Identify the blood parasite species.
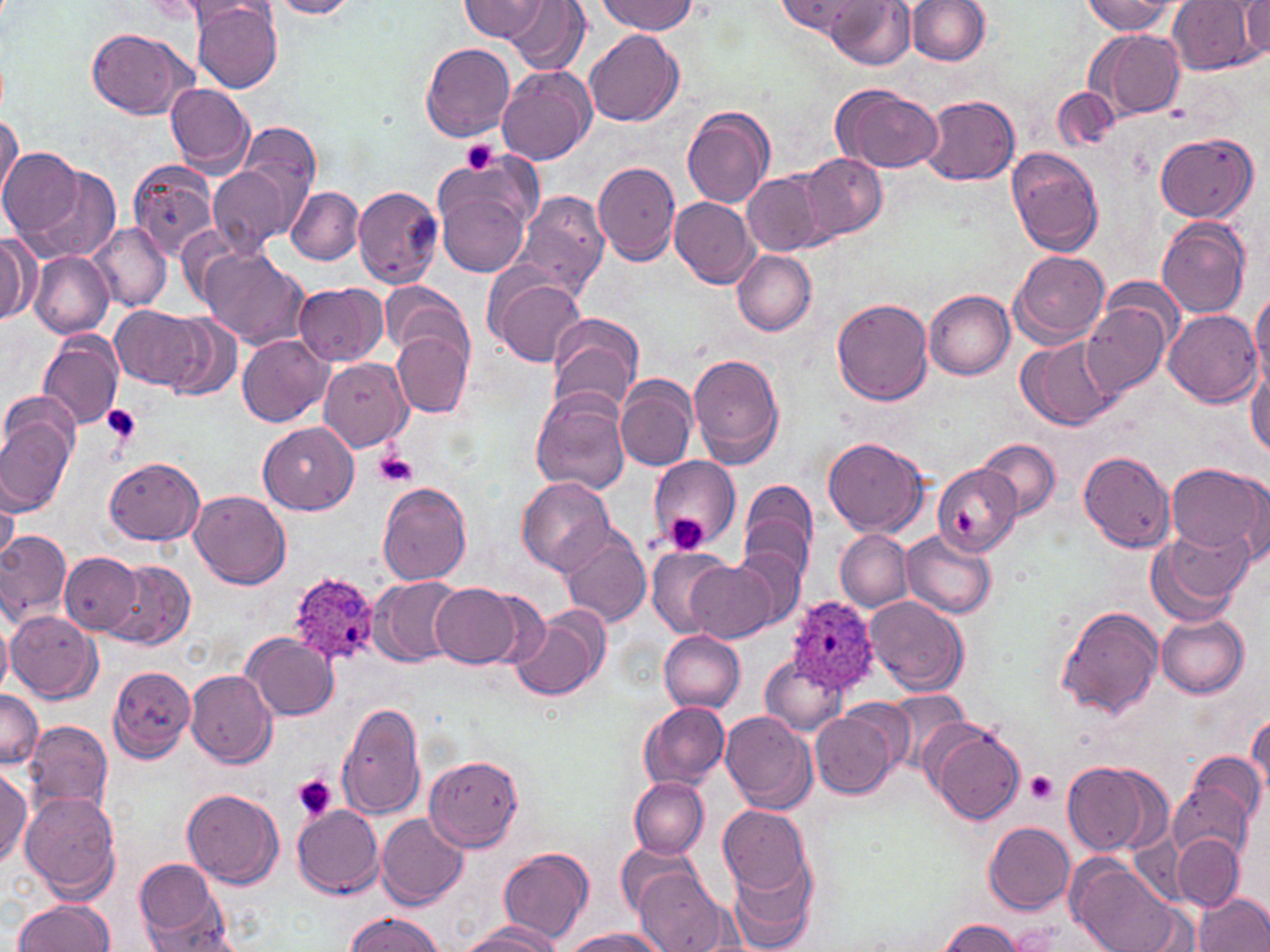
Plasmodium ovale.

image size = 1270×952 pixels
preparation = thin blood smear
uninfected red blood cell locations = approximate bounding boxes as named x1/y1/x2/y2 corners in pixels: (x1=266, y1=0, x2=361, y2=19), (x1=459, y1=0, x2=549, y2=42), (x1=778, y1=0, x2=869, y2=36), (x1=826, y1=0, x2=915, y2=69), (x1=906, y1=0, x2=989, y2=65), (x1=1169, y1=0, x2=1263, y2=75), (x1=506, y1=1, x2=590, y2=76), (x1=597, y1=1, x2=697, y2=35), (x1=1080, y1=1, x2=1178, y2=36), (x1=1240, y1=1, x2=1269, y2=57), (x1=160, y1=2, x2=264, y2=34), (x1=190, y1=2, x2=283, y2=92), (x1=87, y1=26, x2=195, y2=120), (x1=1087, y1=28, x2=1186, y2=121), (x1=584, y1=29, x2=684, y2=126), (x1=421, y1=40, x2=515, y2=142), (x1=498, y1=66, x2=596, y2=165), (x1=166, y1=83, x2=256, y2=174), (x1=831, y1=84, x2=941, y2=173), (x1=1051, y1=88, x2=1120, y2=152), (x1=922, y1=94, x2=1020, y2=186), (x1=682, y1=106, x2=776, y2=209), (x1=0, y1=112, x2=21, y2=209), (x1=218, y1=122, x2=322, y2=243), (x1=1156, y1=132, x2=1257, y2=222), (x1=1007, y1=147, x2=1105, y2=257), (x1=0, y1=148, x2=95, y2=246), (x1=434, y1=153, x2=537, y2=243), (x1=798, y1=153, x2=887, y2=242), (x1=128, y1=160, x2=220, y2=260), (x1=27, y1=161, x2=120, y2=263), (x1=594, y1=161, x2=682, y2=265), (x1=742, y1=170, x2=828, y2=256), (x1=437, y1=185, x2=529, y2=276), (x1=353, y1=186, x2=443, y2=288), (x1=287, y1=187, x2=364, y2=264), (x1=508, y1=189, x2=609, y2=303), (x1=670, y1=197, x2=760, y2=288), (x1=1157, y1=218, x2=1251, y2=319), (x1=88, y1=222, x2=172, y2=311), (x1=1, y1=232, x2=36, y2=325), (x1=199, y1=248, x2=310, y2=350), (x1=1010, y1=249, x2=1110, y2=346), (x1=732, y1=250, x2=817, y2=335), (x1=30, y1=251, x2=113, y2=338), (x1=488, y1=274, x2=586, y2=368), (x1=295, y1=283, x2=389, y2=366), (x1=378, y1=284, x2=473, y2=361), (x1=1250, y1=289, x2=1270, y2=392), (x1=924, y1=290, x2=1015, y2=380), (x1=1081, y1=298, x2=1173, y2=398), (x1=832, y1=299, x2=932, y2=406), (x1=111, y1=306, x2=209, y2=394), (x1=1164, y1=311, x2=1262, y2=408), (x1=547, y1=312, x2=644, y2=415), (x1=161, y1=316, x2=244, y2=403), (x1=39, y1=329, x2=125, y2=432), (x1=393, y1=332, x2=472, y2=417), (x1=237, y1=334, x2=334, y2=427), (x1=1018, y1=336, x2=1119, y2=431), (x1=688, y1=354, x2=786, y2=468), (x1=319, y1=359, x2=413, y2=453), (x1=1246, y1=359, x2=1270, y2=458), (x1=616, y1=377, x2=698, y2=471), (x1=530, y1=389, x2=630, y2=495), (x1=0, y1=411, x2=76, y2=515), (x1=259, y1=421, x2=358, y2=515), (x1=824, y1=437, x2=929, y2=536), (x1=977, y1=439, x2=1061, y2=519), (x1=1078, y1=451, x2=1177, y2=553), (x1=648, y1=455, x2=740, y2=548), (x1=106, y1=458, x2=204, y2=544), (x1=1166, y1=463, x2=1267, y2=562), (x1=932, y1=464, x2=1021, y2=555), (x1=1240, y1=474, x2=1269, y2=568), (x1=519, y1=477, x2=613, y2=573), (x1=739, y1=479, x2=818, y2=578), (x1=377, y1=482, x2=471, y2=586), (x1=189, y1=490, x2=292, y2=589), (x1=1, y1=491, x2=19, y2=566), (x1=1150, y1=524, x2=1253, y2=623), (x1=901, y1=529, x2=997, y2=619), (x1=556, y1=530, x2=652, y2=628), (x1=837, y1=530, x2=913, y2=610), (x1=0, y1=532, x2=71, y2=624), (x1=645, y1=546, x2=739, y2=638), (x1=732, y1=546, x2=808, y2=630), (x1=60, y1=552, x2=145, y2=636), (x1=106, y1=560, x2=195, y2=650), (x1=685, y1=561, x2=777, y2=643), (x1=370, y1=576, x2=467, y2=668), (x1=431, y1=583, x2=522, y2=667), (x1=867, y1=595, x2=968, y2=694), (x1=1056, y1=605, x2=1162, y2=719), (x1=6, y1=610, x2=101, y2=704), (x1=510, y1=610, x2=606, y2=702), (x1=1156, y1=614, x2=1249, y2=698), (x1=0, y1=619, x2=13, y2=695), (x1=241, y1=631, x2=338, y2=721), (x1=660, y1=631, x2=746, y2=711), (x1=759, y1=655, x2=847, y2=736), (x1=108, y1=665, x2=197, y2=763), (x1=185, y1=669, x2=276, y2=768), (x1=0, y1=688, x2=43, y2=771), (x1=885, y1=689, x2=973, y2=766), (x1=335, y1=701, x2=428, y2=820), (x1=639, y1=703, x2=729, y2=789), (x1=813, y1=708, x2=898, y2=798), (x1=720, y1=711, x2=817, y2=814), (x1=1247, y1=714, x2=1270, y2=799), (x1=25, y1=722, x2=113, y2=814), (x1=930, y1=724, x2=1025, y2=826), (x1=424, y1=753, x2=524, y2=852), (x1=1186, y1=753, x2=1266, y2=834), (x1=1061, y1=760, x2=1170, y2=857), (x1=0, y1=766, x2=31, y2=867), (x1=630, y1=777, x2=709, y2=858), (x1=1169, y1=779, x2=1257, y2=865), (x1=182, y1=786, x2=283, y2=888), (x1=21, y1=792, x2=121, y2=900), (x1=292, y1=805, x2=384, y2=897), (x1=720, y1=808, x2=812, y2=894), (x1=375, y1=812, x2=469, y2=909), (x1=983, y1=821, x2=1075, y2=914), (x1=1173, y1=834, x2=1243, y2=911), (x1=616, y1=842, x2=706, y2=923), (x1=498, y1=846, x2=594, y2=944), (x1=726, y1=852, x2=819, y2=952), (x1=1069, y1=858, x2=1185, y2=952), (x1=136, y1=859, x2=222, y2=940), (x1=635, y1=867, x2=726, y2=951), (x1=1195, y1=893, x2=1270, y2=952), (x1=12, y1=899, x2=115, y2=952), (x1=139, y1=905, x2=236, y2=951), (x1=343, y1=913, x2=445, y2=951), (x1=936, y1=919, x2=1024, y2=952), (x1=458, y1=922, x2=561, y2=951), (x1=562, y1=928, x2=664, y2=952)
Plasmodium ovale-infected red blood cell locations = approximate bounding boxes as named x1/y1/x2/y2 corners in pixels: (x1=288, y1=571, x2=383, y2=668), (x1=787, y1=596, x2=879, y2=694)
modality = optical microscopy
stain = May-Grünwald-Giemsa
field of view = one of a larger specimen
platelet locations = approximate bounding boxes as named x1/y1/x2/y2 corners in pixels: (x1=462, y1=138, x2=500, y2=174), (x1=102, y1=404, x2=142, y2=443), (x1=376, y1=451, x2=416, y2=488), (x1=951, y1=510, x2=975, y2=535), (x1=663, y1=512, x2=709, y2=557), (x1=1026, y1=771, x2=1059, y2=803), (x1=293, y1=775, x2=337, y2=822)
magnification = 1000x